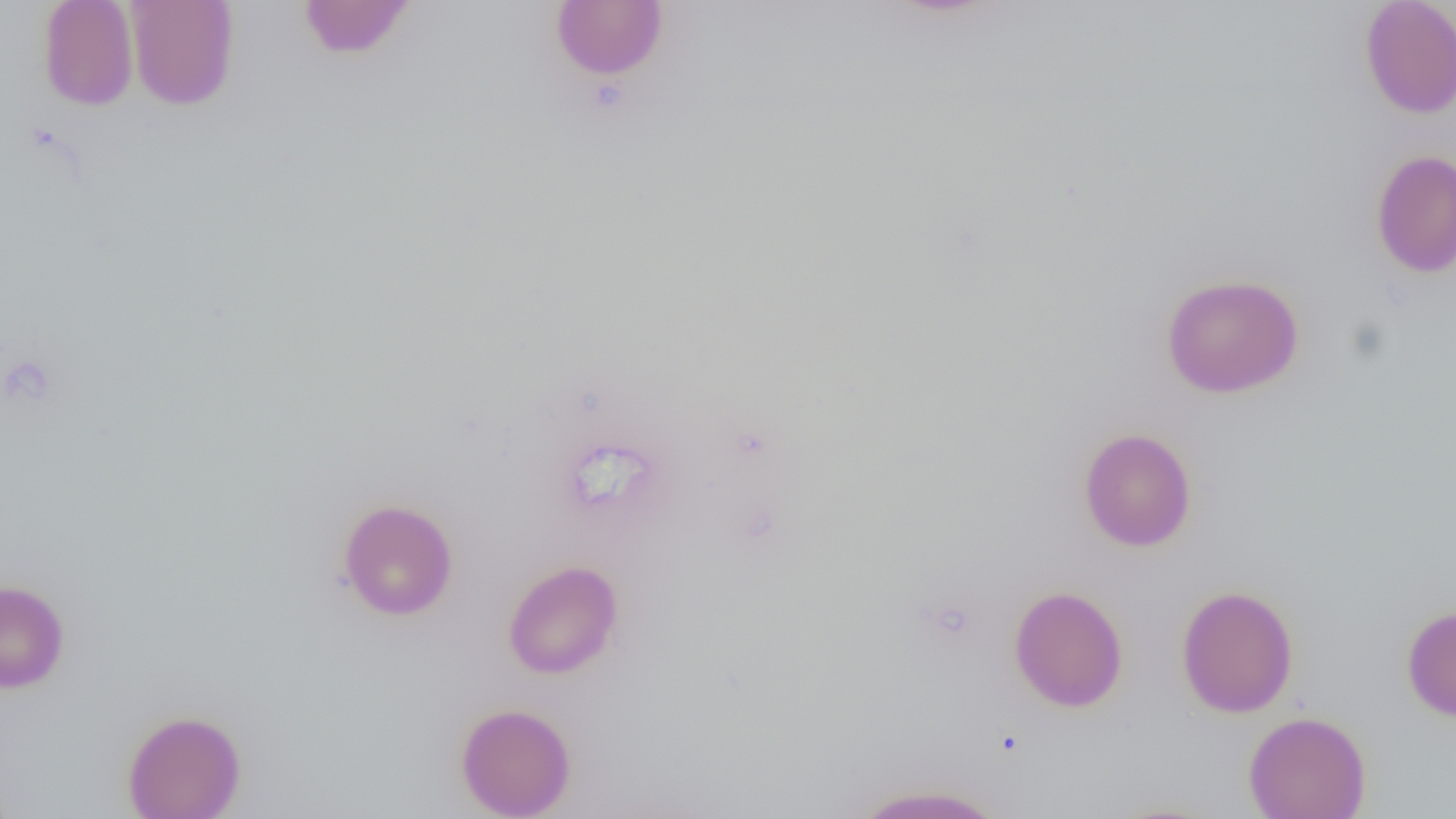
Approximate bounding boxes as named x1/y1/x2/y2 corners in pixels. Uninfected red blood cell locations: (x1=37, y1=0, x2=139, y2=111), (x1=125, y1=0, x2=240, y2=111), (x1=296, y1=0, x2=418, y2=60), (x1=1359, y1=0, x2=1456, y2=118), (x1=548, y1=1, x2=670, y2=81), (x1=1370, y1=150, x2=1456, y2=277), (x1=1160, y1=272, x2=1304, y2=398), (x1=1078, y1=427, x2=1197, y2=552), (x1=336, y1=498, x2=458, y2=621), (x1=503, y1=559, x2=623, y2=679), (x1=0, y1=579, x2=70, y2=693), (x1=1176, y1=584, x2=1299, y2=718), (x1=1008, y1=585, x2=1129, y2=712), (x1=1401, y1=603, x2=1456, y2=722), (x1=455, y1=702, x2=577, y2=818), (x1=122, y1=709, x2=247, y2=818), (x1=1243, y1=711, x2=1371, y2=819), (x1=848, y1=782, x2=1008, y2=819). Slide-level diagnosis: negative for blood parasites. One field of a larger specimen. Thin blood film. Image is 1456×819 pixels. Optical microscopy. Captured at 1000x magnification.